Give the extent of all uninfected red blood cells.
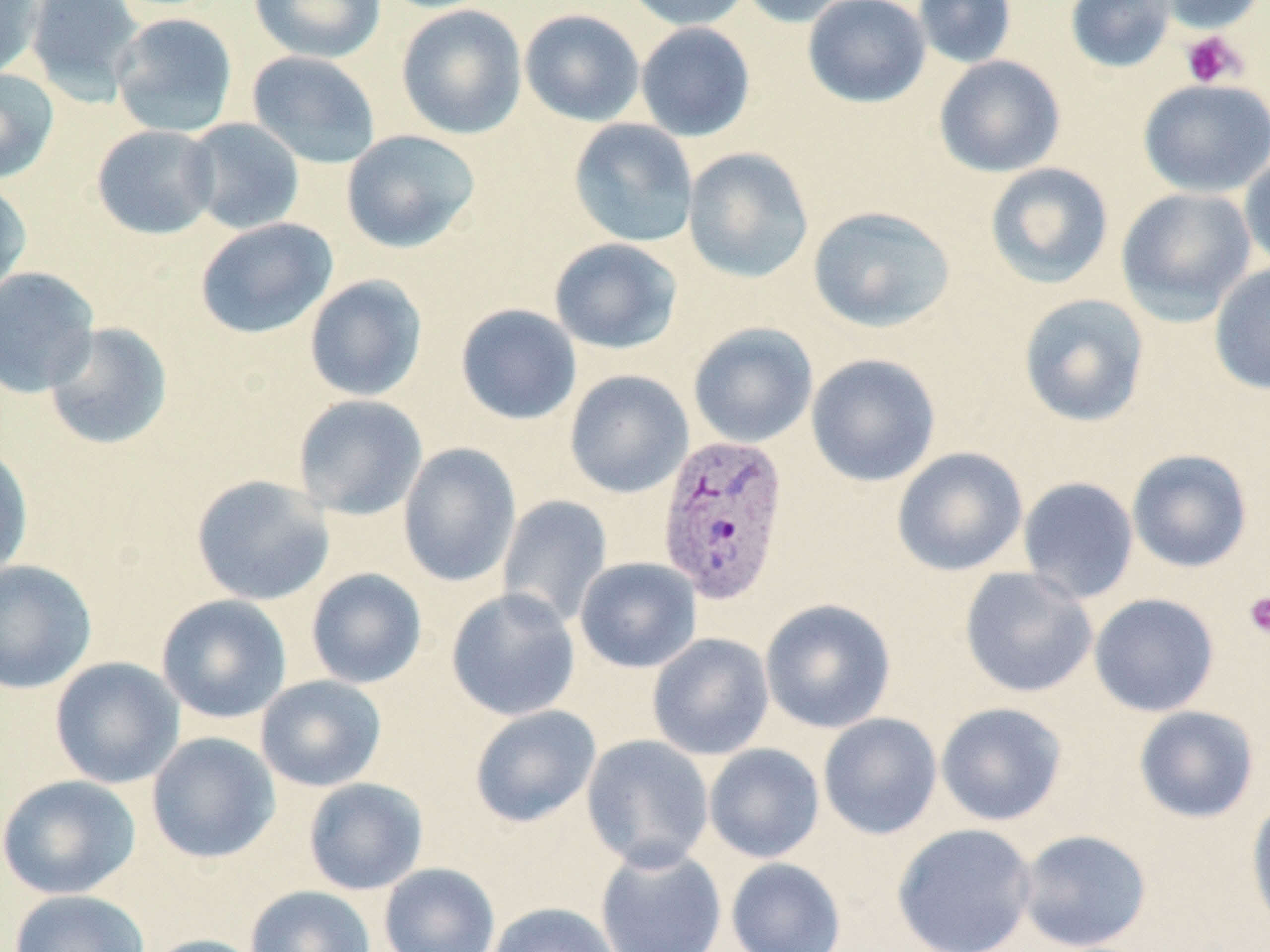

Approximate bounding boxes as (x1,y1)-(x2,y2) corner pairs in pixels.
Uninfected red blood cells: (0,0)-(44,80), (25,0)-(145,104), (249,0)-(385,63), (622,0)-(752,31), (736,0)-(857,27), (802,0)-(931,108), (912,0)-(1017,69), (1064,0)-(1177,74), (1150,0)-(1265,34), (395,4)-(528,140), (519,9)-(645,127), (110,12)-(239,138), (635,22)-(756,142), (246,50)-(381,169), (933,55)-(1066,178), (0,68)-(59,185), (1137,78)-(1270,198), (183,117)-(305,235), (568,118)-(699,248), (91,124)-(220,240), (341,129)-(481,253), (682,146)-(814,284), (1239,152)-(1270,275), (984,162)-(1114,290), (0,179)-(32,300), (1115,187)-(1257,323), (808,205)-(955,333), (195,217)-(338,340), (549,238)-(683,355), (1208,262)-(1270,395), (0,266)-(100,398), (303,274)-(428,402), (1017,293)-(1150,427), (455,303)-(582,425), (43,321)-(174,451), (687,322)-(818,448), (805,353)-(941,487), (564,369)-(693,498), (292,394)-(428,520), (0,441)-(34,581), (398,442)-(521,586), (891,447)-(1027,576), (1127,449)-(1253,573), (190,474)-(335,606), (1017,476)-(1139,604), (497,495)-(612,628), (574,557)-(702,673), (0,559)-(97,694), (959,566)-(1098,698), (305,568)-(427,689), (445,588)-(581,721), (1089,593)-(1219,717), (156,594)-(292,724), (759,598)-(896,733), (647,632)-(775,761), (49,657)-(185,789), (255,674)-(387,792), (935,701)-(1068,826), (469,704)-(601,827), (1133,705)-(1260,823), (818,712)-(942,840), (146,732)-(280,864), (581,734)-(714,871), (704,743)-(825,863), (0,774)-(141,899), (303,777)-(428,895), (1246,797)-(1270,933), (892,822)-(1038,952), (1016,829)-(1152,951), (594,843)-(727,952), (726,857)-(846,952), (378,862)-(500,952), (245,885)-(376,952), (9,889)-(150,952), (486,901)-(621,952), (142,934)-(268,952).

Platelet locations: (1181,31)-(1247,88), (1243,591)-(1270,639). Plasmodium vivax-infected red blood cell locations: (657,432)-(790,607). Slide-level diagnosis: Plasmodium vivax. Light microscopy. 1000x magnification. May-Grünwald-Giemsa-stained preparation. Thin blood film. Image is 1270×952 pixels. Single field of view.